Classify this cell by malaria status.
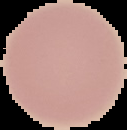
It is uninfected.

Summary:
  - Image size: 127×130 pixels
  - Image type: cell region segmented out of the field of view; surrounding area masked to black
  - Preparation: thin blood smear